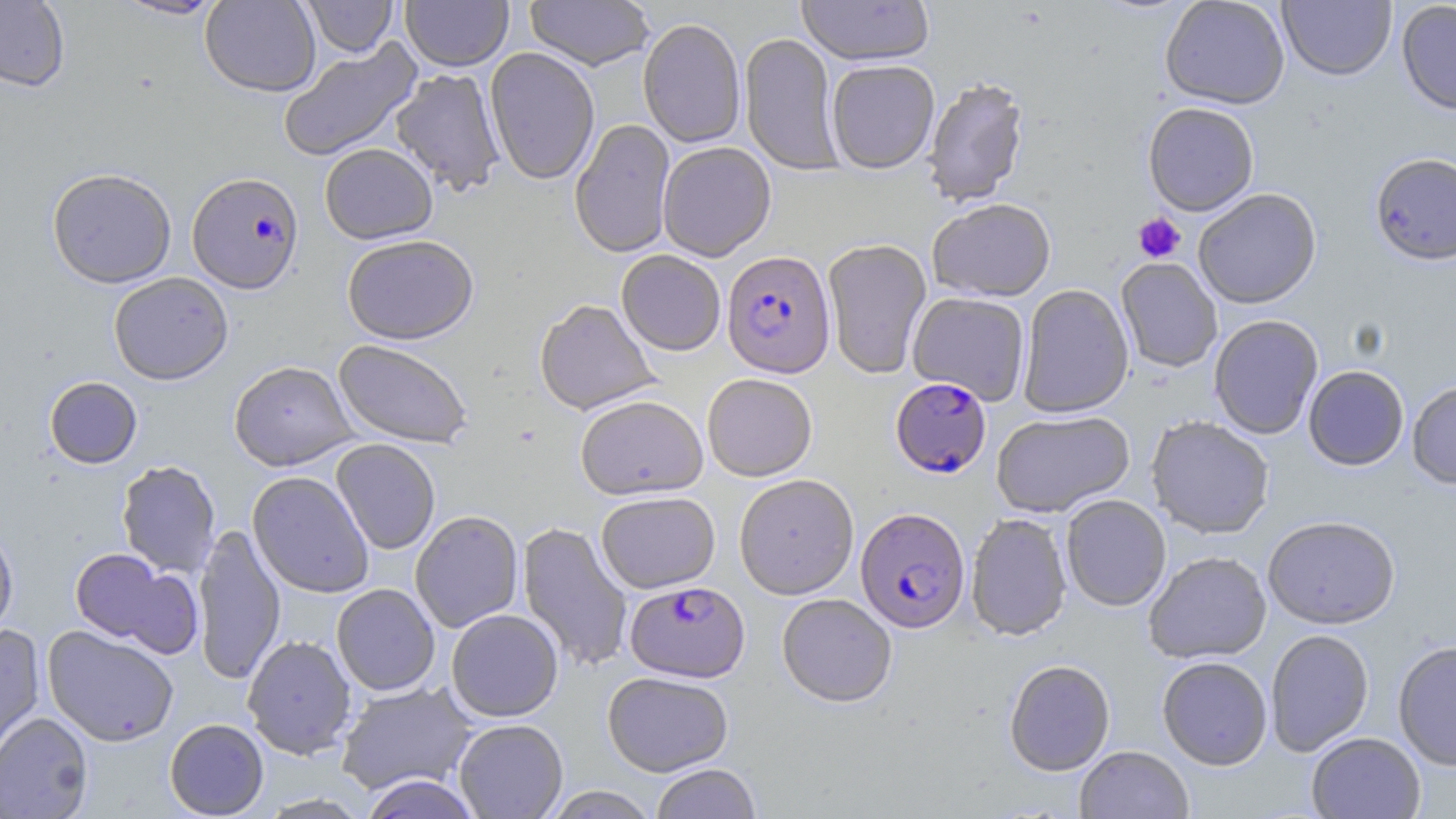
slide-level diagnosis = Plasmodium falciparum
modality = light microscopy
stain = May-Grünwald-Giemsa
preparation = thin blood film
image size = 1456×819 pixels
uninfected red blood cell locations = approximate bounding boxes as (x1, y1, x2, y2) in pixels: (0, 0, 70, 91), (113, 0, 226, 20), (200, 0, 321, 96), (302, 0, 398, 57), (401, 0, 513, 71), (525, 0, 654, 71), (797, 0, 935, 67), (1160, 0, 1290, 109), (1278, 0, 1396, 81), (1396, 0, 1456, 116), (638, 18, 746, 148), (739, 32, 842, 175), (277, 39, 422, 162), (484, 47, 600, 185), (826, 59, 940, 174), (390, 68, 506, 197), (922, 77, 1030, 208), (1142, 102, 1259, 217), (570, 119, 675, 259), (658, 142, 776, 261), (319, 143, 438, 244), (1370, 153, 1456, 266), (47, 167, 177, 288), (1193, 189, 1322, 309), (928, 198, 1056, 302), (342, 234, 479, 345), (822, 238, 932, 379), (616, 250, 726, 355), (1116, 258, 1223, 373), (108, 272, 233, 385), (1017, 284, 1134, 419), (908, 292, 1031, 405), (534, 299, 659, 415), (1208, 314, 1324, 440), (333, 339, 473, 449), (229, 360, 357, 471), (1303, 365, 1409, 470), (702, 373, 818, 481), (44, 377, 142, 468), (1407, 381, 1456, 489), (575, 394, 707, 500), (992, 411, 1134, 518), (1146, 416, 1274, 539), (331, 439, 441, 555), (116, 460, 221, 576), (247, 471, 374, 598), (734, 474, 859, 599), (596, 491, 720, 593), (1061, 495, 1171, 611), (410, 510, 524, 632), (965, 513, 1072, 641), (1263, 516, 1400, 630), (517, 521, 633, 672), (0, 523, 19, 643), (192, 523, 286, 686), (69, 548, 201, 656), (1143, 551, 1272, 664), (331, 583, 440, 696), (777, 593, 897, 707), (447, 609, 563, 722), (0, 625, 46, 762), (42, 625, 179, 746), (1265, 629, 1374, 757), (242, 634, 357, 759), (1393, 641, 1456, 771), (1157, 656, 1272, 771), (1004, 659, 1115, 777), (602, 671, 734, 776), (335, 681, 477, 795), (0, 712, 94, 819), (165, 718, 269, 818), (454, 719, 568, 818), (1307, 732, 1426, 819), (1076, 745, 1194, 819), (651, 763, 761, 819), (360, 775, 481, 819), (542, 786, 659, 818)
platelet locations = approximate bounding boxes as (x1, y1, x2, y2) in pixels: (1133, 212, 1186, 263)
magnification = 1000x
Plasmodium falciparum-infected red blood cell locations = approximate bounding boxes as (x1, y1, x2, y2) in pixels: (187, 171, 304, 294), (721, 250, 836, 379), (890, 377, 991, 478), (856, 507, 970, 633), (625, 581, 749, 682)
field of view = one of a larger specimen